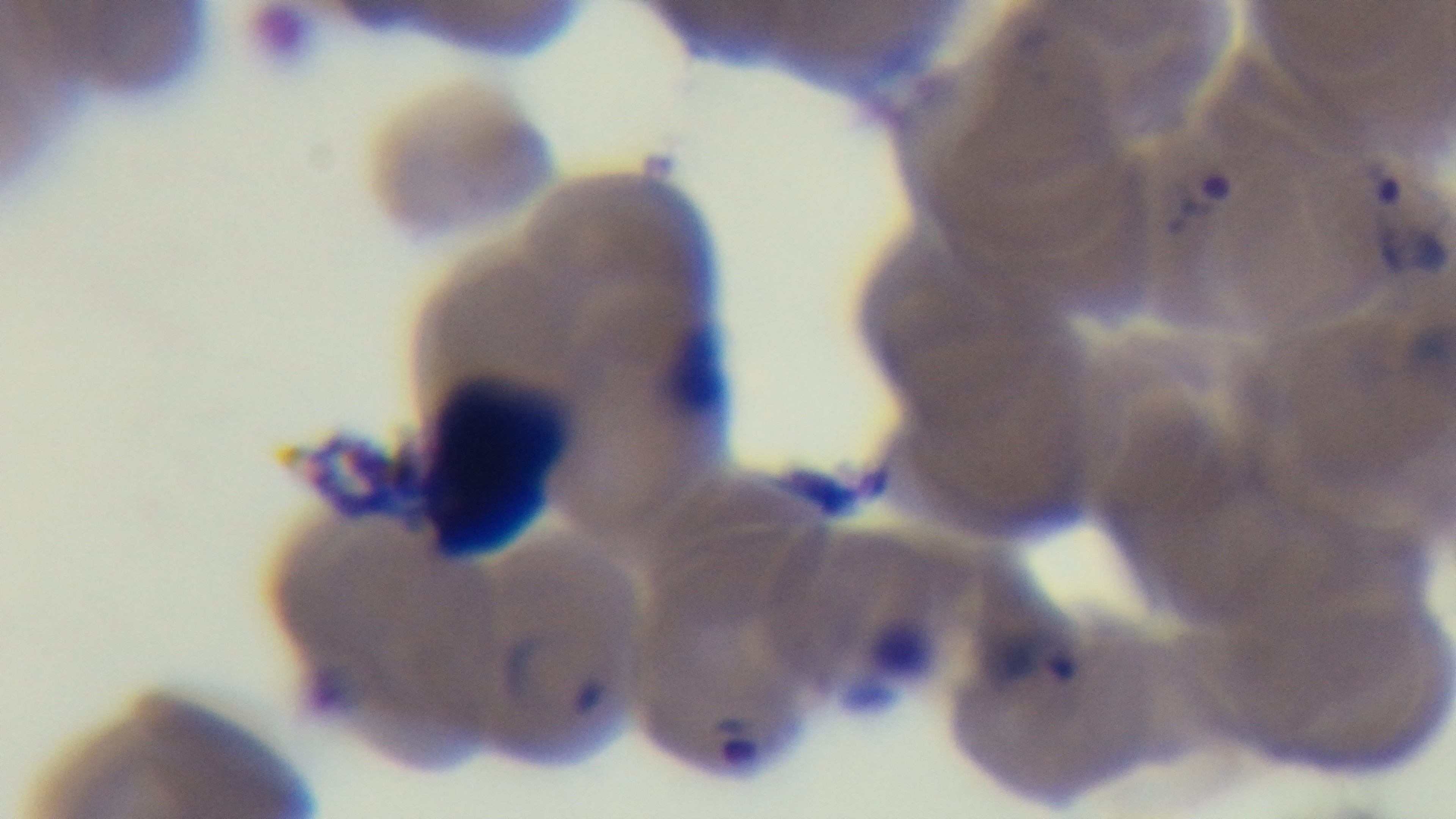

Giemsa stain. Preparation: thin smear. Mounted 4K digital camera. Malaria status: infected. Oil-immersion objective, 100x. One field from the slide. Photomicrograph.